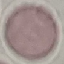

Summary:
  - Result: no malaria parasites seen
  - Stain: Giemsa
  - Preparation: thin smear
  - Image type: automatically extracted cell patch, resized to 64 × 64 pixels
  - Capture: smartphone through the microscope eyepiece